Name the parasite shown.
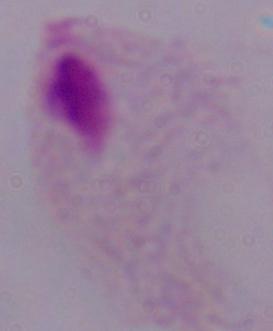

This is a trichomonad.

Summary:
  - Modality: micrograph
  - Magnification: 1000x